Assess this cell for malaria.
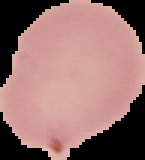
Parasitized.

Segmented cell region on a black background. Image is 145×160 pixels. From a thin blood smear.